Describe the morphology of the erythrocytes.
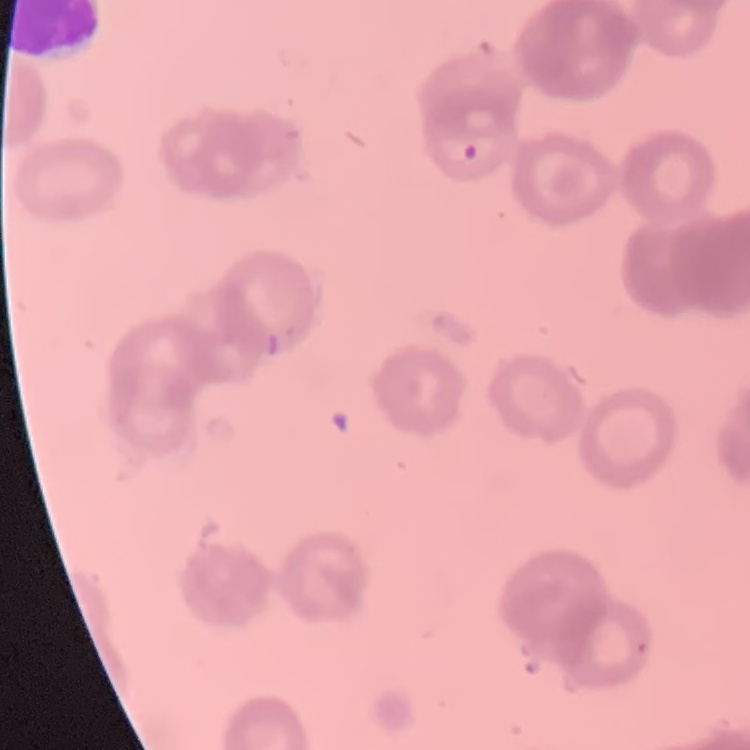

Rouleaux formation.

Summary:
  - Preparation: thin peripheral smear
  - Stain: Field's or Giemsa
  - Image type: square crop of a larger photomicrograph